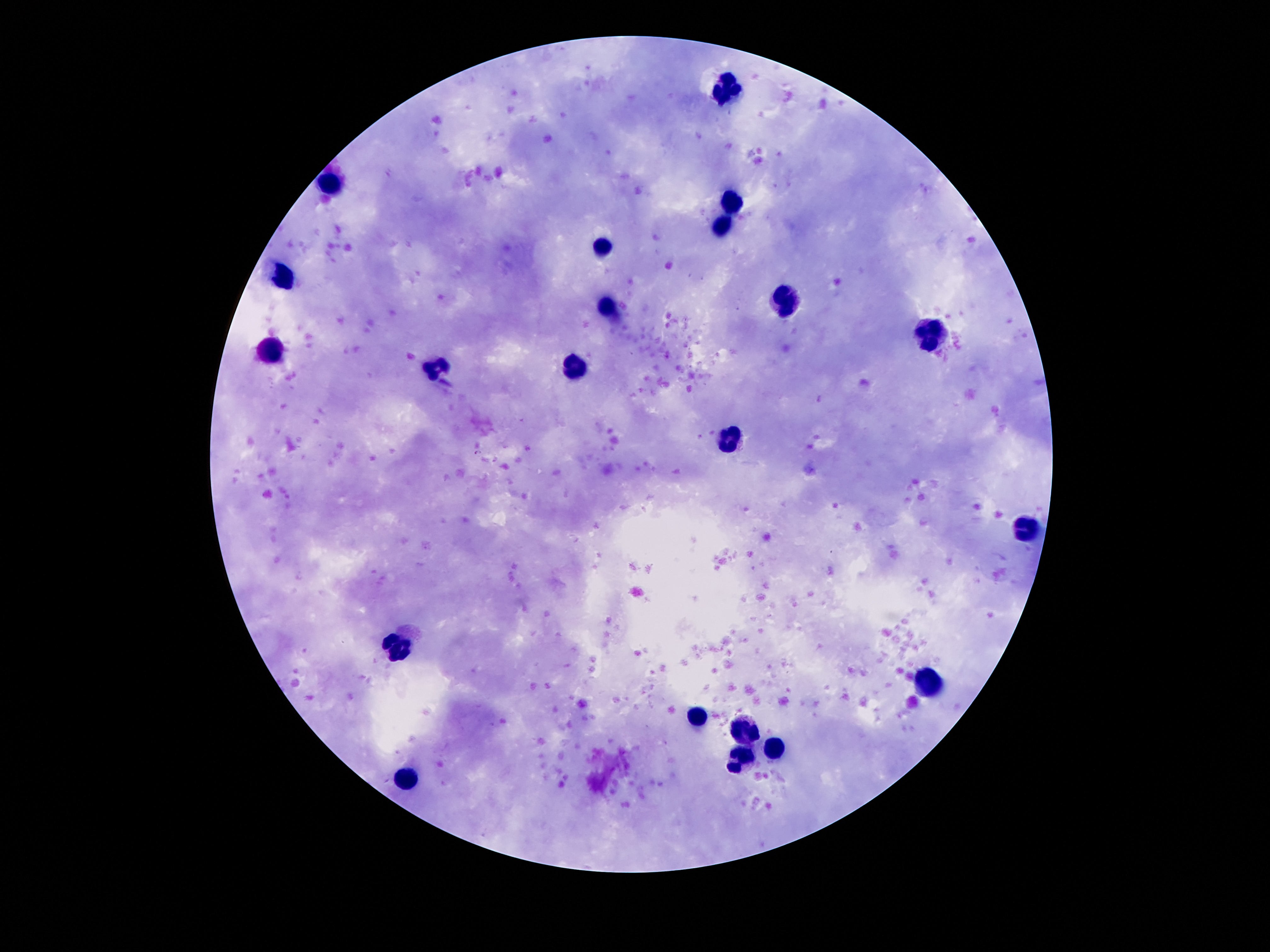
magnification: 100x
field_of_view: single
capture: smartphone camera through the microscope eyepiece
stain: Giemsa
image_size: 1270×952 pixels
patient_malaria_status: not infected
leukocyte_locations: 'approximate object centers, in pixels from the top-left corner: (x=726, y=85), (x=329, y=181), (x=733, y=200), (x=720, y=227), (x=602, y=246), (x=283, y=275), (x=789, y=299), (x=606, y=307), (x=932, y=332), (x=268, y=355), (x=581, y=364), (x=436, y=372), (x=733, y=440), (x=1027, y=531), (x=401, y=648), (x=926, y=680), (x=697, y=716), (x=745, y=731), (x=779, y=745), (x=741, y=760), (x=405, y=780)'
preparation: thick blood smear